State the preparation type.
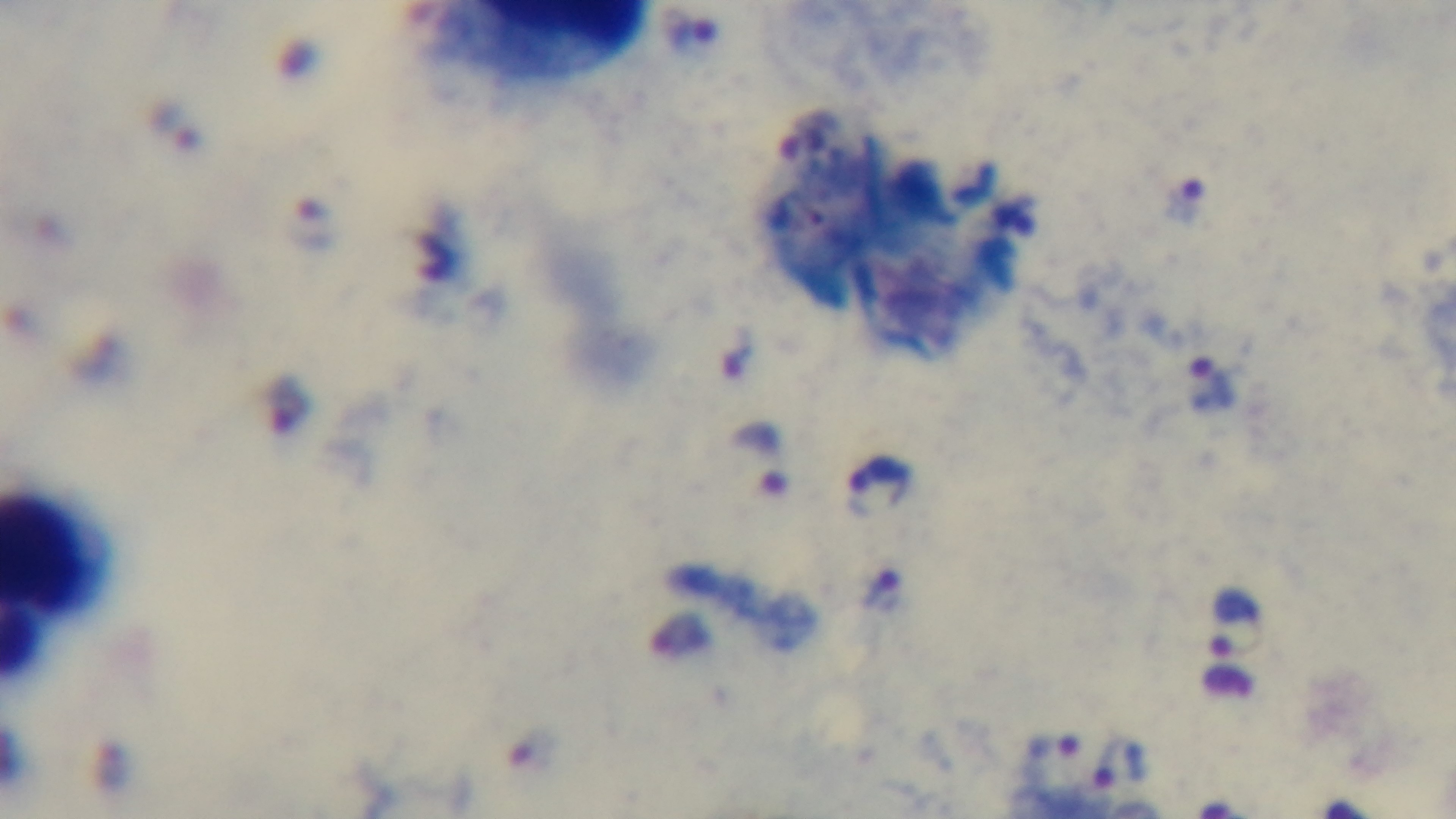
It is a thick blood film.

Summary:
  - Modality: light microscopy
  - Malaria status: positive
  - Stain: Giemsa
  - Objective: 100x oil immersion
  - Capture: mounted 4K digital camera
  - Field of view: one from the slide